Report the malaria status of this cell.
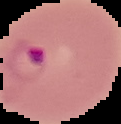

Parasitized.

Summary:
  - Preparation: thin blood smear
  - Image size: 121×124 pixels
  - Image type: segmented cell region on a black background